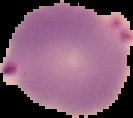
Cell region segmented out of the field of view; the surrounding area is masked to black. Image is 133×118 pixels. Malaria status: parasitized. From a thin blood film.